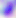
Micrograph. 400x magnification. Toxoplasma gondii is seen.